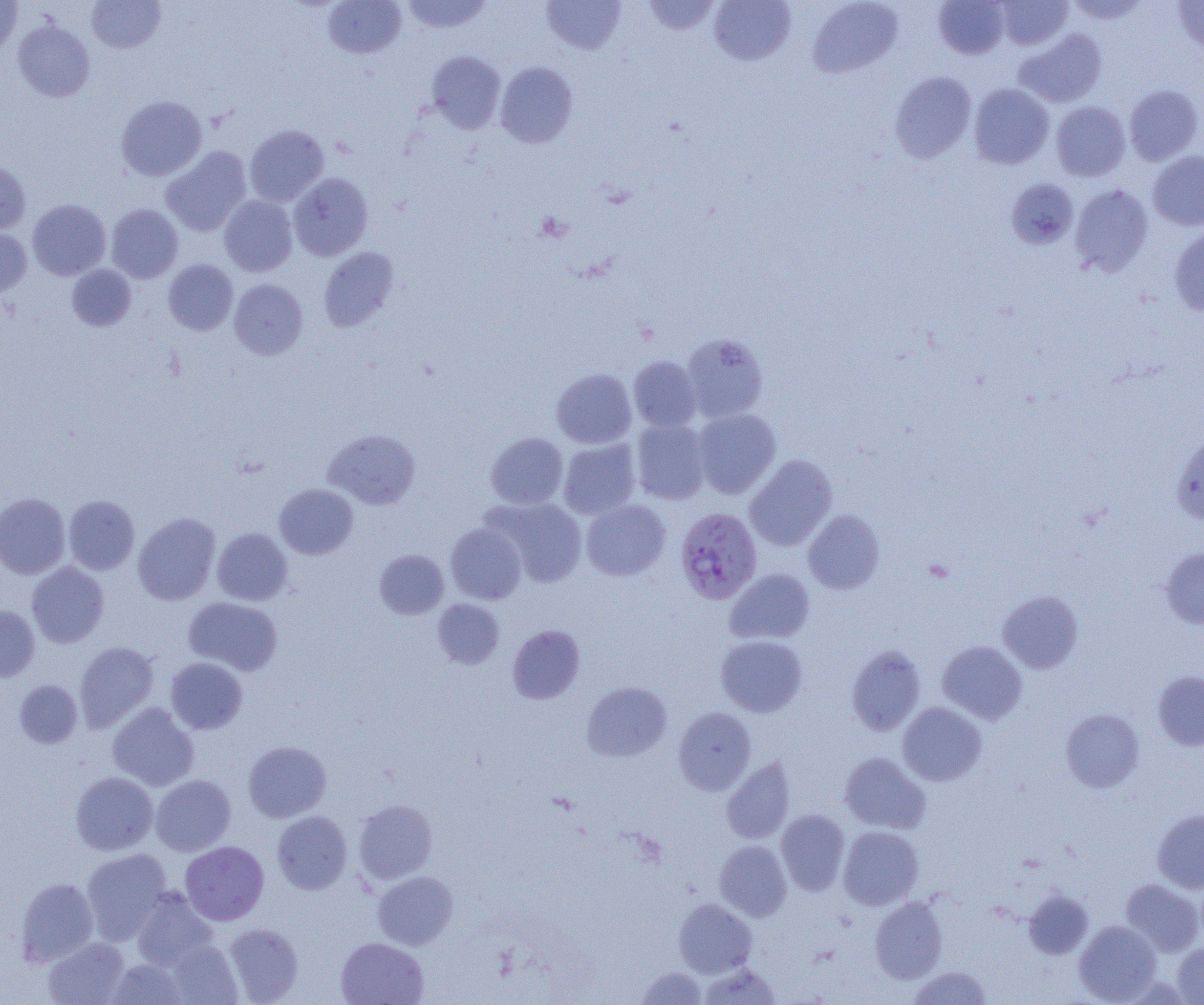
Summary:
  - Coordinate format: approximate bounding boxes as (x1, y1, x2, y2) in pixels
  - Uninfected red blood cell locations: (0, 0, 23, 55), (86, 0, 165, 52), (323, 0, 406, 59), (401, 0, 493, 34), (542, 0, 626, 54), (642, 0, 722, 35), (709, 0, 795, 65), (808, 0, 904, 77), (933, 0, 1010, 59), (1062, 0, 1150, 25), (994, 1, 1073, 51), (1173, 1, 1204, 55), (13, 20, 95, 102), (1014, 28, 1107, 108), (426, 50, 506, 134), (495, 61, 578, 148), (890, 72, 977, 163), (969, 83, 1054, 169), (1124, 84, 1203, 165), (116, 96, 207, 181), (1051, 101, 1130, 181), (244, 125, 329, 207), (161, 146, 251, 236), (1147, 151, 1204, 231), (0, 160, 30, 235), (288, 173, 372, 261), (1006, 178, 1079, 249), (1070, 184, 1153, 276), (219, 195, 297, 276), (27, 199, 110, 280), (106, 204, 183, 283), (1169, 225, 1204, 315), (0, 227, 32, 297), (318, 247, 399, 332), (164, 259, 238, 335), (67, 264, 136, 331), (229, 279, 307, 360), (681, 333, 768, 422), (628, 356, 702, 431), (551, 368, 636, 448), (692, 408, 781, 499), (631, 419, 711, 505), (324, 429, 421, 509), (1170, 429, 1204, 525), (486, 432, 568, 509), (558, 439, 640, 519), (744, 455, 837, 551), (274, 483, 358, 559), (0, 493, 70, 579), (63, 495, 139, 575), (485, 497, 588, 587), (581, 500, 670, 581), (803, 509, 884, 594), (133, 513, 220, 605), (446, 523, 527, 604), (212, 528, 292, 605), (1161, 547, 1204, 629), (374, 549, 449, 619), (27, 561, 109, 647), (725, 569, 815, 645), (998, 591, 1083, 673), (184, 597, 282, 676), (432, 599, 504, 669), (0, 605, 40, 681), (507, 624, 584, 703), (716, 635, 807, 717), (75, 641, 158, 732), (937, 641, 1027, 724), (846, 646, 925, 735), (165, 657, 247, 734), (1153, 671, 1204, 751), (14, 680, 82, 748), (581, 681, 672, 761), (108, 702, 198, 791), (898, 702, 987, 786), (673, 707, 756, 794), (1060, 709, 1144, 792), (243, 741, 331, 822), (839, 752, 931, 834), (722, 757, 795, 844), (71, 771, 158, 855), (151, 775, 236, 856), (353, 799, 438, 884), (776, 809, 850, 895), (1152, 809, 1204, 894), (272, 810, 352, 894), (838, 826, 924, 910), (180, 841, 269, 925), (715, 841, 792, 921), (81, 849, 172, 944), (372, 871, 458, 949), (16, 877, 99, 966), (1121, 878, 1204, 956), (131, 888, 218, 971), (1023, 889, 1093, 959), (870, 896, 947, 983), (674, 898, 757, 977), (1074, 920, 1161, 1004), (224, 923, 304, 1004), (43, 937, 130, 1005), (336, 937, 428, 1005), (166, 939, 243, 1004), (1172, 942, 1204, 1004), (107, 958, 189, 1004), (699, 962, 781, 1004), (636, 966, 708, 1004), (909, 966, 992, 1005)
  - Plasmodium falciparum-infected red blood cell locations: (675, 507, 762, 605)
  - Slide-level diagnosis: Plasmodium falciparum
  - Modality: light microscopy
  - Image size: 1204×1005 pixels
  - Magnification: 1000x
  - Preparation: thin blood film
  - Field of view: single